Point out each malaria parasite.
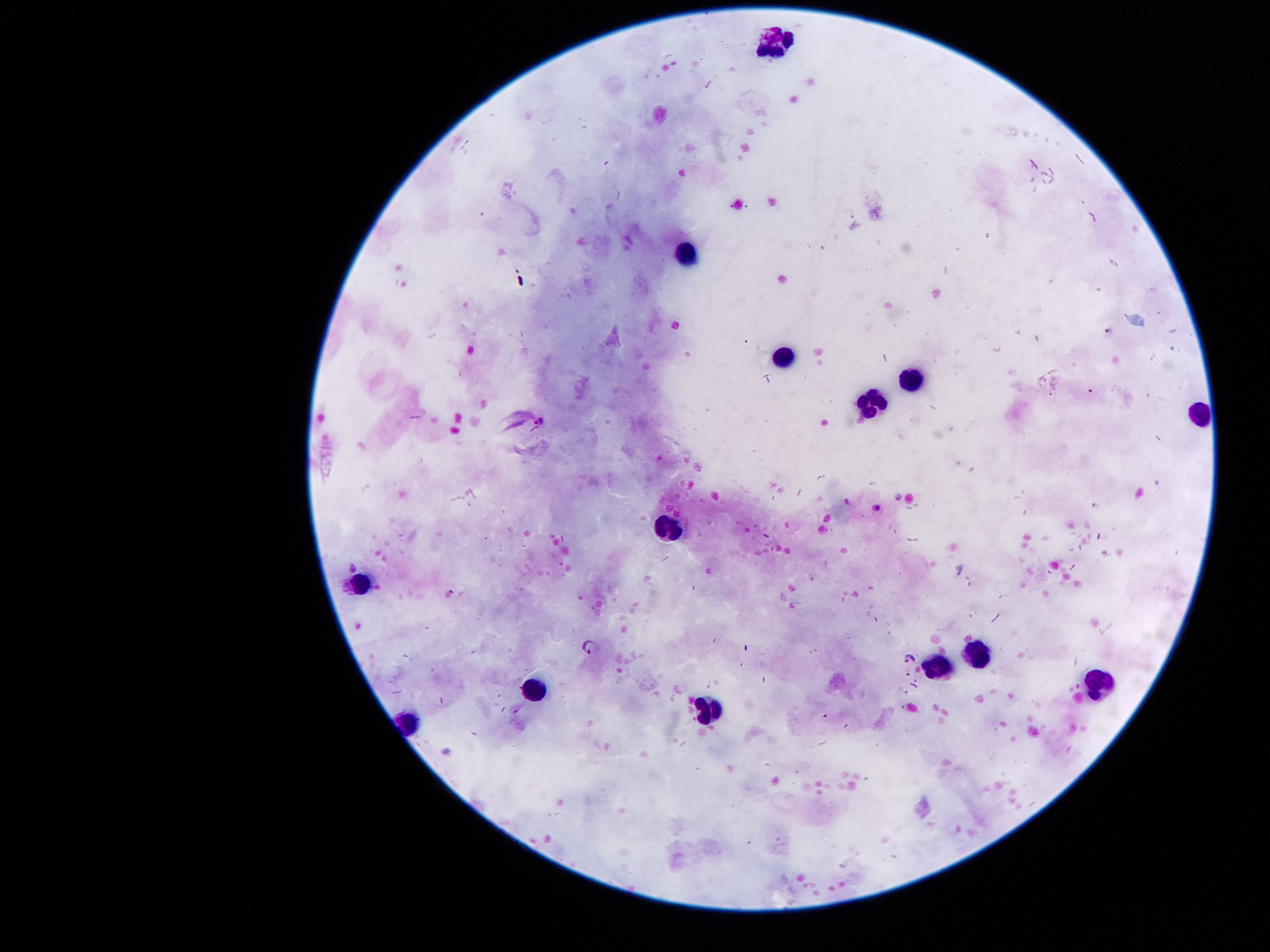

Approximate centers as {x, y} in pixels.
Malaria parasites: {540, 420}, {878, 505}, {590, 648}, {912, 660}.

Summary:
  - Leukocyte locations: {775, 39}, {684, 255}, {782, 361}, {903, 378}, {866, 414}, {1199, 415}, {665, 527}, {358, 587}, {983, 656}, {936, 667}, {1100, 684}, {526, 689}, {706, 710}
  - Magnification: 100x
  - Capture: smartphone through the microscope eyepiece
  - Image size: 1270×952 pixels
  - Preparation: thick blood smear
  - Patient malaria status: infected with Plasmodium falciparum
  - Stain: Giemsa
  - Field of view: one from this slide